Assess the morphology of the red blood cells.
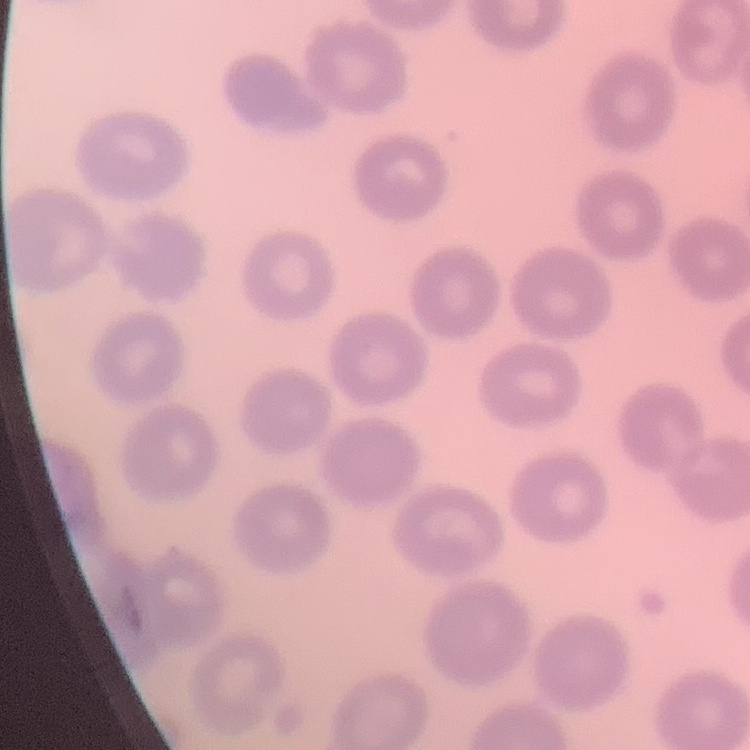
No rouleaux formation.

image type = square crop of a larger photomicrograph
stain = Field's or Giemsa
preparation = thin blood film